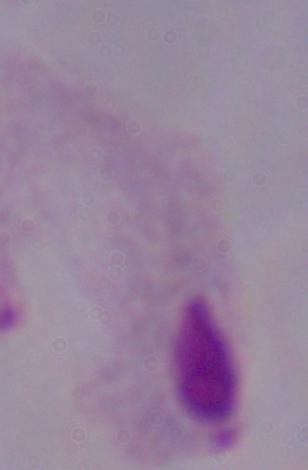 A trichomonad is seen. Captured at 1000x magnification. Micrograph.